Locate every blood parasite and identify its species.
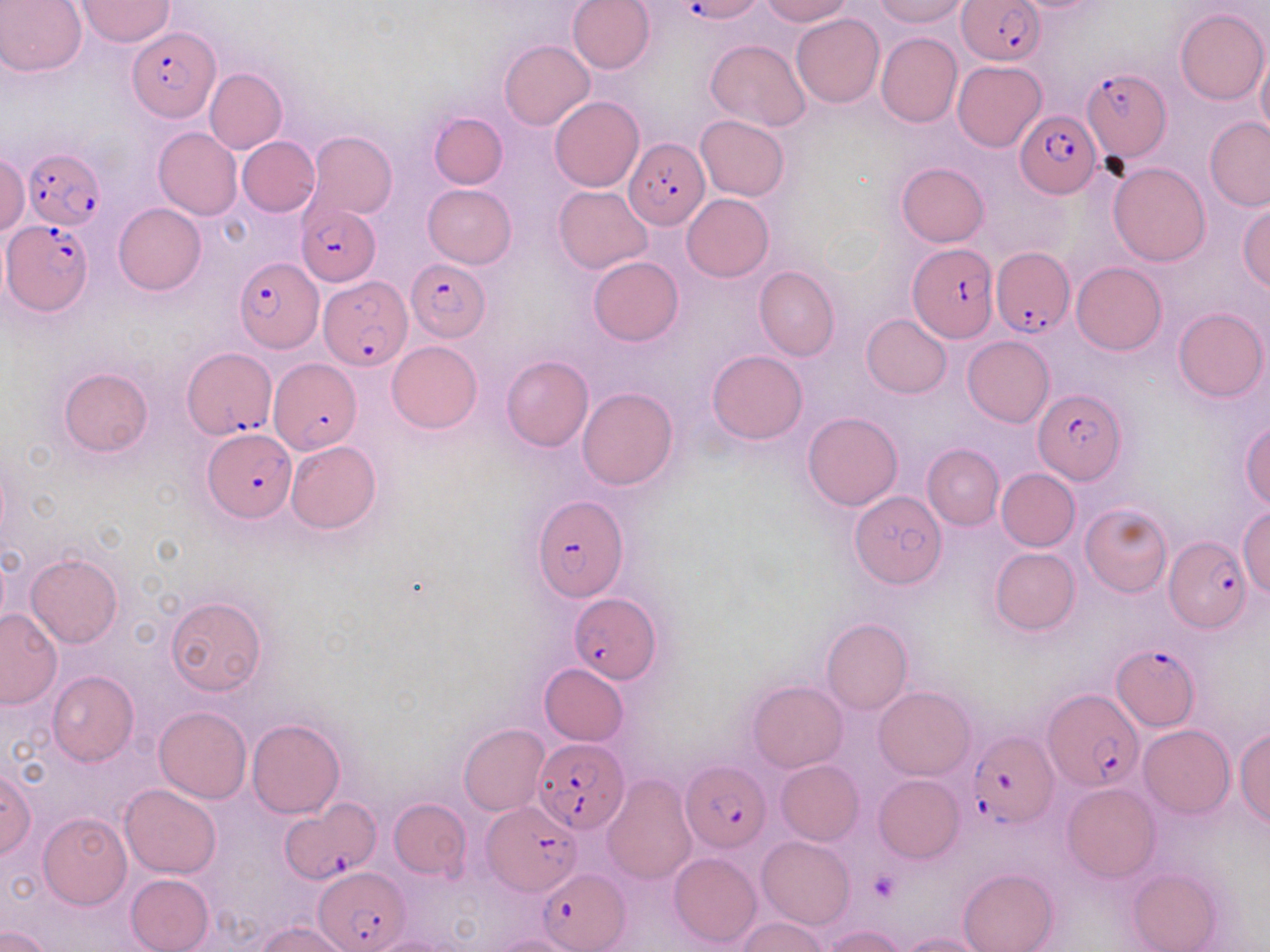
Approximate bounding boxes as (x1,y1)-(x2,y2) corner pairs in pixels.
Plasmodium falciparum-infected red blood cells: (678,1)-(751,23), (958,1)-(1045,64), (128,26)-(219,121), (1081,68)-(1171,166), (1016,109)-(1099,196), (624,136)-(710,231), (21,147)-(103,232), (297,205)-(380,286), (2,220)-(92,315), (908,243)-(998,343), (990,247)-(1072,338), (234,258)-(322,351), (405,260)-(491,342), (318,275)-(410,371), (182,346)-(277,441), (266,358)-(359,454), (1034,387)-(1126,484), (205,430)-(295,520), (532,496)-(628,601), (1162,533)-(1252,631), (570,597)-(660,683), (1111,643)-(1201,730), (1044,690)-(1142,792), (966,729)-(1056,826), (533,737)-(628,833), (681,761)-(770,850), (482,800)-(583,895), (278,801)-(380,884), (316,867)-(411,950), (539,868)-(629,950).
No Plasmodium ovale, Plasmodium malariae, Plasmodium vivax, Babesia divergens, or Trypanosoma brucei observed.

Summary:
  - Platelet locations: (870,872)-(900,902)
  - Uninfected red blood cell locations: (1,0)-(86,76), (567,0)-(655,74), (758,0)-(852,25), (872,0)-(970,27), (75,1)-(174,47), (1174,8)-(1269,106), (790,13)-(884,107), (875,32)-(962,128), (706,39)-(810,132), (500,40)-(594,130), (1257,44)-(1270,145), (952,60)-(1047,152), (204,67)-(287,154), (550,96)-(644,192), (429,112)-(508,189), (696,115)-(790,200), (1205,116)-(1270,212), (152,127)-(241,220), (301,131)-(397,223), (237,136)-(320,216), (0,154)-(28,236), (896,161)-(989,246), (1108,162)-(1212,266), (424,184)-(516,268), (553,185)-(654,274), (682,194)-(773,281), (1238,200)-(1270,291), (114,203)-(206,295), (587,256)-(683,345), (1072,261)-(1167,355), (754,267)-(839,360), (1173,306)-(1267,402), (861,313)-(952,397), (962,336)-(1054,428), (386,340)-(482,433), (707,349)-(808,445), (501,355)-(594,451), (59,367)-(153,456), (577,387)-(678,490), (802,412)-(903,511), (1242,420)-(1270,510), (286,440)-(381,534), (922,444)-(1005,530), (996,468)-(1080,550), (849,490)-(945,589), (1081,503)-(1172,597), (1238,507)-(1270,597), (990,547)-(1080,635), (25,553)-(123,647), (165,595)-(267,697), (0,608)-(63,708), (821,618)-(912,716), (540,663)-(628,745), (48,669)-(139,766), (748,680)-(847,772), (875,686)-(975,780), (154,706)-(251,804), (246,717)-(345,819), (458,724)-(549,816), (1138,724)-(1234,818), (1234,727)-(1270,828), (775,760)-(864,845), (0,767)-(37,858), (602,773)-(697,883), (873,775)-(963,862), (1063,783)-(1159,881), (120,784)-(221,877), (389,799)-(471,880), (38,812)-(131,908), (757,836)-(854,930), (669,852)-(762,949), (958,867)-(1058,952), (1129,868)-(1221,952), (125,874)-(214,952), (738,918)-(829,952), (258,922)-(351,952), (821,925)-(907,952), (1,927)-(53,952), (899,932)-(989,952), (491,934)-(580,952), (359,935)-(458,952)
  - Slide-level diagnosis: Plasmodium falciparum
  - Modality: optical microscopy
  - Preparation: thin blood film
  - Image size: 1270×952 pixels
  - Field of view: single
  - Magnification: 1000x
  - Stain: May-Grünwald-Giemsa